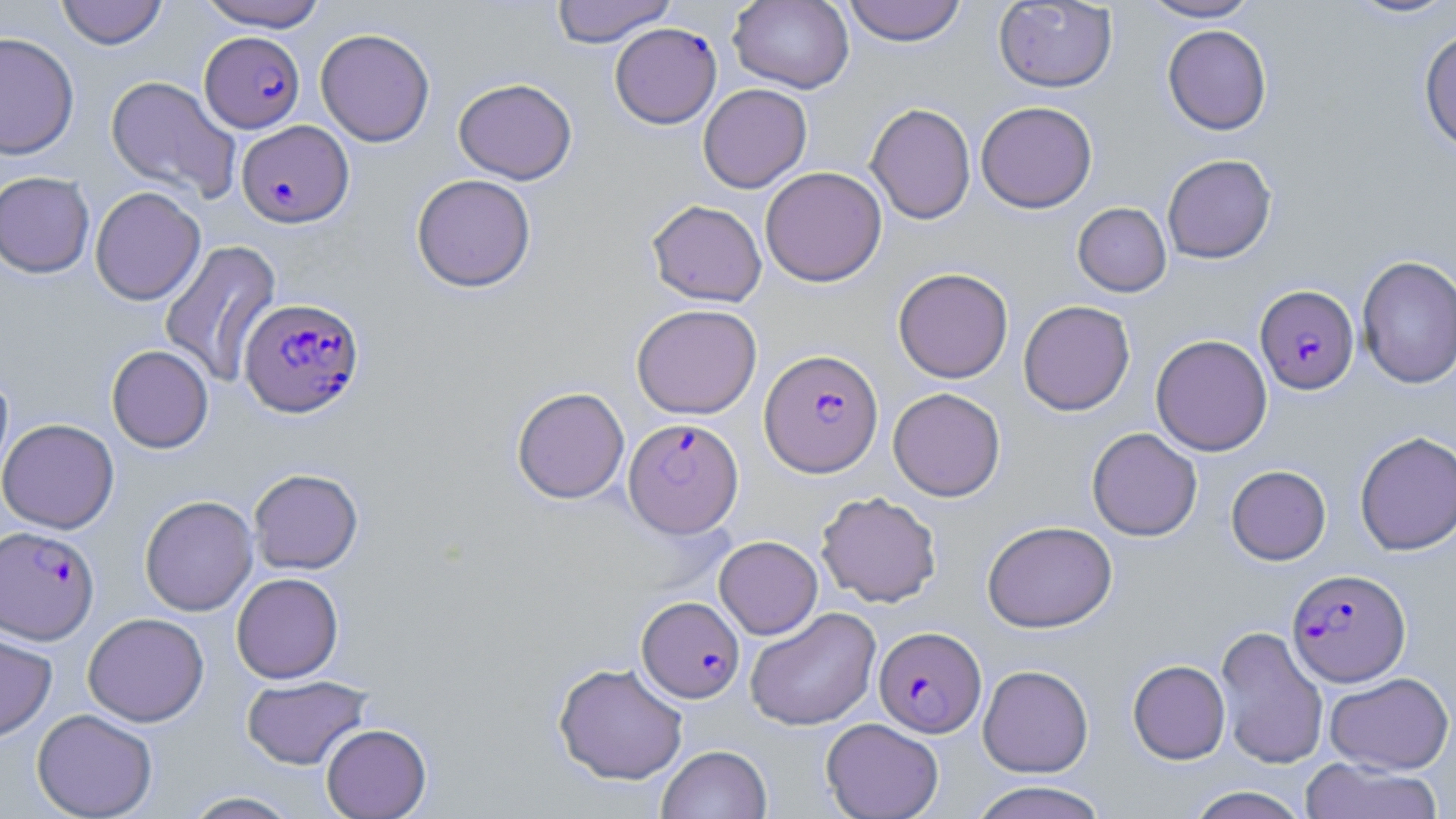
Summary:
  - Coordinate format: approximate bounding boxes as (x1, y1, x2, y2) in pixels
  - Plasmodium falciparum-infected red blood cell locations: (609, 23, 722, 128), (200, 31, 305, 133), (236, 120, 353, 228), (1255, 285, 1359, 395), (239, 298, 364, 418), (759, 349, 884, 477), (624, 418, 743, 537), (0, 525, 99, 644), (1287, 568, 1410, 685), (636, 596, 744, 703), (874, 626, 986, 737)
  - Uninfected red blood cell locations: (55, 0, 168, 49), (197, 0, 327, 31), (551, 0, 677, 47), (728, 0, 854, 93), (843, 0, 966, 46), (1138, 0, 1261, 22), (1343, 0, 1456, 20), (994, 1, 1117, 92), (1162, 24, 1272, 135), (1419, 26, 1456, 154), (315, 27, 435, 147), (0, 31, 80, 160), (105, 76, 241, 202), (453, 78, 577, 184), (698, 83, 812, 193), (976, 101, 1097, 213), (865, 103, 976, 225), (1162, 154, 1277, 263), (760, 166, 887, 287), (0, 171, 95, 277), (411, 173, 536, 292), (90, 186, 206, 305), (646, 199, 767, 306), (1072, 202, 1171, 297), (158, 239, 282, 387), (1357, 254, 1456, 389), (893, 267, 1013, 383), (1018, 300, 1135, 416), (631, 303, 762, 419), (1151, 334, 1272, 456), (106, 345, 214, 453), (0, 368, 14, 491), (511, 387, 630, 504), (888, 387, 1006, 501), (0, 418, 119, 533), (1087, 428, 1202, 541), (1354, 431, 1456, 555), (1226, 465, 1331, 565), (248, 468, 363, 574), (816, 491, 942, 607), (139, 495, 258, 616), (982, 520, 1117, 633), (714, 535, 823, 639), (231, 572, 344, 683), (744, 607, 881, 731), (83, 612, 209, 727), (1214, 625, 1328, 769), (0, 628, 57, 742), (1127, 660, 1230, 764), (553, 661, 689, 785), (978, 664, 1093, 777), (1325, 671, 1454, 774), (241, 675, 372, 770), (32, 708, 158, 819), (821, 717, 944, 819), (320, 723, 431, 818), (656, 744, 772, 819), (1298, 757, 1445, 819), (968, 780, 1110, 819), (1184, 786, 1310, 819), (180, 791, 302, 818)
  - Slide-level diagnosis: Plasmodium falciparum
  - Magnification: 1000x
  - Stain: May-Grünwald-Giemsa
  - Preparation: thin blood film
  - Field of view: one of a larger specimen
  - Modality: optical microscopy
  - Image size: 1456×819 pixels